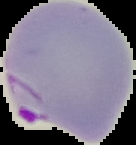
Summary:
  - Image type: segmented cell region on a black background
  - Malaria status: parasitized
  - Preparation: thin blood smear
  - Image size: 136×145 pixels